Assess this cell for malaria.
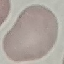
It is uninfected.

Thin blood film. Acquired by smartphone through the microscope eyepiece. Giemsa stain. Automatically extracted cell patch, resized to 64 × 64 pixels.